Assess this cell for malaria.
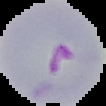

It is parasitized.

Image is 106×106 pixels. From a thin blood film. The area outside the segmented cell region is set to black.